State which parasite is depicted.
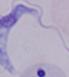
A trypanosome.

modality = photomicrograph
magnification = 1000x